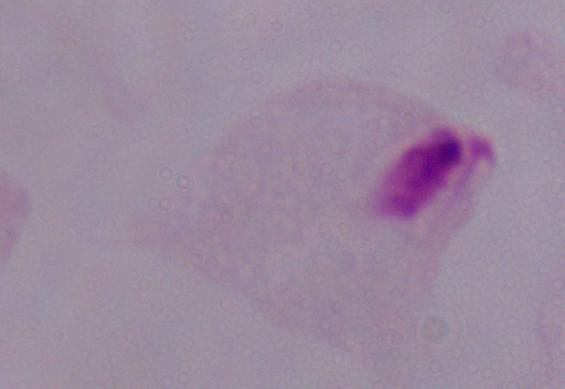
magnification = 1000x
identification = trichomonad
modality = photomicrograph